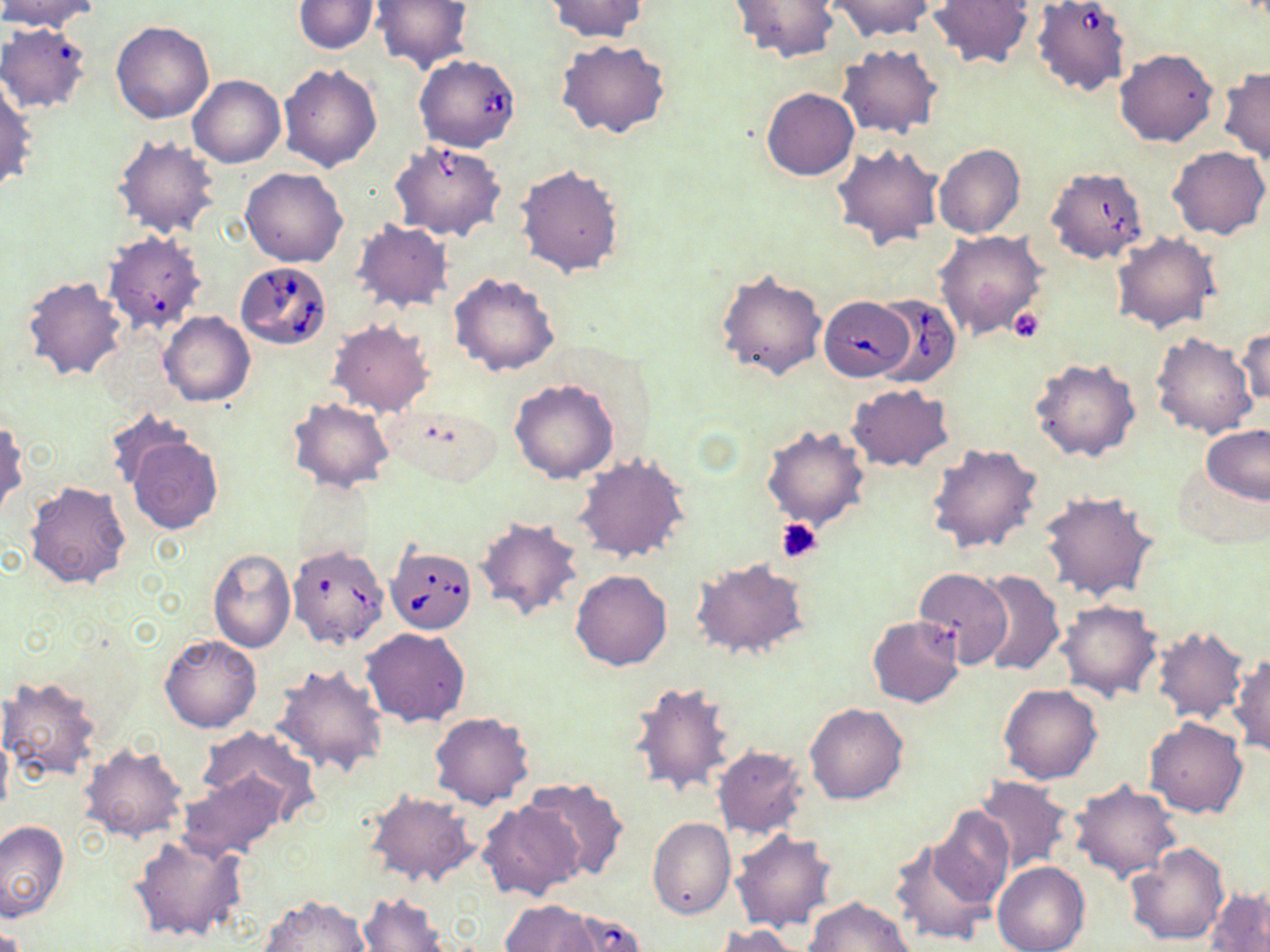

{
  "slide_level_diagnosis": "Babesia divergens",
  "platelet_locations": "approximate bounding boxes as (x1, y1, x2, y2) in pixels: (1008, 307, 1045, 343), (775, 517, 821, 562)",
  "preparation": "thin blood smear",
  "field_of_view": "one of a larger specimen",
  "babesia_divergens_infected_red_blood_cell_locations": "approximate bounding boxes as (x1, y1, x2, y2) in pixels: (1035, 2, 1130, 99), (414, 53, 521, 153), (1048, 164, 1149, 268), (99, 233, 206, 334), (235, 259, 332, 349), (869, 293, 961, 387), (818, 296, 914, 381), (386, 546, 476, 633), (286, 554, 389, 650)",
  "stain": "May-Grünwald-Giemsa",
  "modality": "optical microscopy",
  "magnification": "1000x",
  "uninfected_red_blood_cell_locations": "approximate bounding boxes as (x1, y1, x2, y2) in pixels: (1, 0, 102, 33), (291, 0, 381, 54), (372, 0, 473, 72), (545, 0, 648, 42), (728, 0, 841, 63), (927, 0, 1036, 70), (827, 1, 934, 41), (111, 21, 214, 124), (0, 23, 92, 113), (557, 40, 669, 140), (836, 44, 943, 139), (1116, 49, 1218, 148), (278, 64, 382, 173), (1217, 67, 1270, 162), (187, 75, 285, 168), (0, 78, 37, 194), (761, 88, 858, 181), (112, 134, 220, 237), (391, 139, 507, 242), (831, 143, 943, 251), (934, 144, 1025, 239), (1167, 146, 1269, 239), (516, 165, 624, 278), (241, 168, 347, 267), (352, 219, 453, 313), (934, 230, 1048, 342), (1111, 230, 1220, 333), (715, 268, 827, 383), (20, 273, 128, 383), (449, 273, 561, 376), (159, 312, 255, 407), (328, 320, 434, 417), (1238, 321, 1269, 410), (1150, 332, 1257, 439), (1031, 356, 1142, 461), (510, 379, 619, 483), (846, 383, 954, 471), (289, 398, 394, 492), (103, 407, 202, 498), (0, 419, 27, 518), (761, 424, 870, 532), (1201, 425, 1270, 504), (122, 428, 223, 534), (926, 442, 1044, 555), (574, 453, 690, 563), (1171, 463, 1266, 549), (23, 480, 132, 589), (294, 482, 379, 565), (1038, 490, 1160, 603), (473, 516, 584, 623), (207, 548, 295, 653), (689, 557, 813, 662), (913, 567, 1012, 669), (570, 569, 672, 671), (974, 570, 1064, 677), (1056, 600, 1162, 700), (866, 615, 964, 708), (1151, 624, 1250, 725), (361, 627, 471, 728), (159, 634, 261, 733), (1231, 654, 1270, 755), (273, 662, 387, 778), (0, 676, 103, 782), (628, 680, 736, 799), (999, 683, 1102, 783), (804, 703, 908, 805), (429, 711, 535, 809), (1145, 717, 1249, 818), (196, 724, 321, 819), (0, 728, 12, 821), (711, 744, 808, 837), (80, 745, 190, 842), (177, 771, 287, 860), (974, 776, 1074, 875), (524, 777, 629, 881), (1069, 780, 1181, 882), (364, 791, 478, 886), (478, 799, 585, 901), (930, 806, 1014, 912), (648, 817, 736, 919), (0, 820, 69, 921), (730, 830, 838, 932), (131, 832, 247, 944), (890, 832, 1000, 947), (1125, 843, 1229, 946), (994, 861, 1089, 952), (1205, 886, 1270, 952), (357, 892, 453, 952), (256, 894, 373, 952), (805, 897, 915, 951), (501, 900, 600, 951), (557, 908, 647, 951), (714, 924, 807, 952)",
  "image_size": "1270×952 pixels"
}